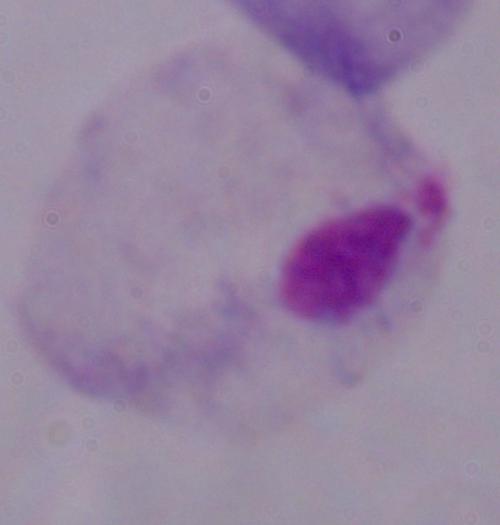

magnification = 1000x
modality = photomicrograph
identification = trichomonad